Point out malaria parasites and leukocytes.
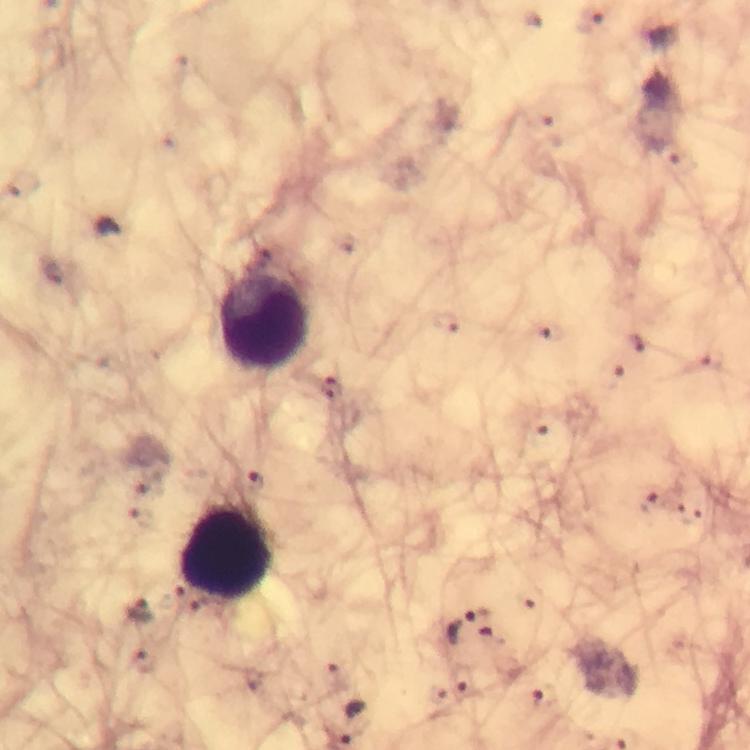

Approximate object centers, in pixels from the top-left corner.
Malaria parasites: (x=589, y=22), (x=445, y=323), (x=619, y=378), (x=332, y=390), (x=539, y=424), (x=254, y=482), (x=648, y=504), (x=689, y=517), (x=466, y=625), (x=140, y=658), (x=463, y=682), (x=543, y=698).
Leukocytes: (x=264, y=322), (x=226, y=554).

Image is 750×750 pixels. 100x magnification. Giemsa-stained preparation. Cropped region of a single field of view. From a diagnostic examination for malaria. Smartphone photograph taken through a microscope. Thick blood film. Immersion oil applied.